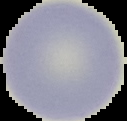

{
  "malaria_status": "uninfected",
  "image_size": "127×121 pixels",
  "image_type": "cell region segmented out of the field of view; surrounding area masked to black",
  "preparation": "thin blood film"
}